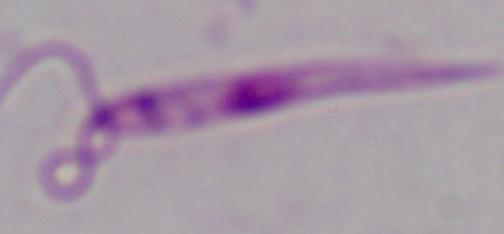

identification = Leishmania
magnification = 1000x
modality = photomicrograph